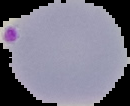
Segmented cell region on a black background. Image is 130×106 pixels. Result: Plasmodium parasites identified. From a thin blood smear.